Name the cell type shown.
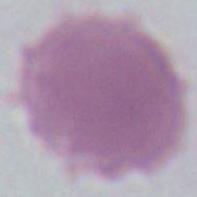

An erythrocyte.

magnification: 1000x
modality: micrograph